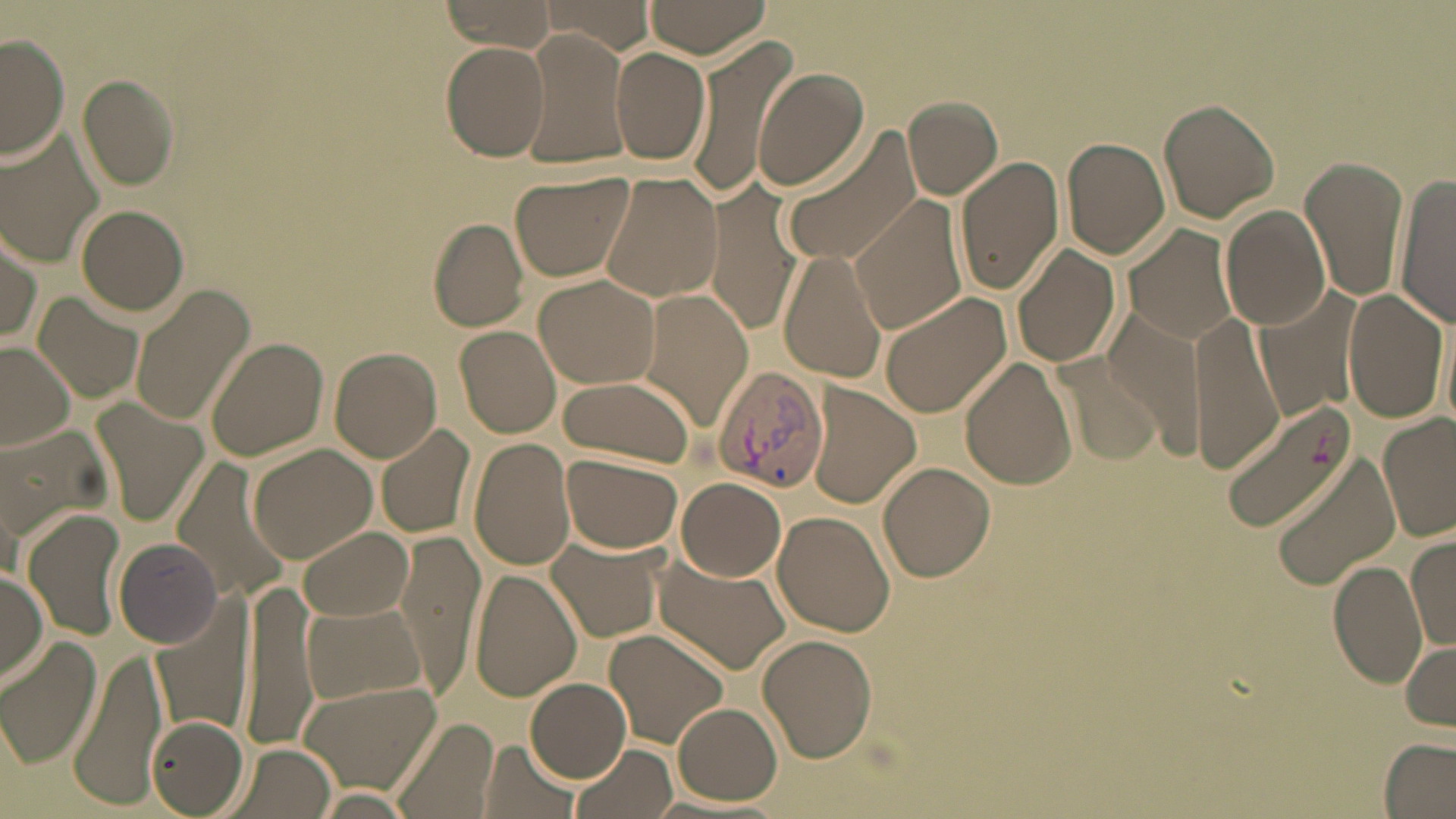

slide-level diagnosis = Plasmodium vivax
stain = May-Grünwald-Giemsa
uninfected red blood cell locations = approximate bounding boxes as [x1, y1, x2, y2] in pixels: [439, 0, 553, 55], [536, 0, 657, 53], [640, 0, 772, 58], [684, 31, 798, 204], [517, 33, 628, 170], [0, 34, 70, 162], [441, 42, 550, 160], [611, 49, 711, 166], [755, 68, 868, 191], [78, 73, 184, 190], [902, 96, 1002, 199], [1158, 100, 1278, 224], [777, 129, 925, 268], [0, 130, 107, 270], [1063, 138, 1169, 259], [1300, 154, 1408, 303], [955, 157, 1065, 294], [510, 169, 635, 282], [598, 173, 723, 302], [1394, 176, 1455, 328], [707, 183, 805, 336], [847, 196, 967, 335], [76, 205, 190, 316], [1223, 205, 1333, 331], [426, 218, 530, 331], [1122, 223, 1243, 344], [0, 228, 43, 346], [1011, 244, 1120, 369], [778, 249, 890, 384], [534, 275, 661, 389], [129, 283, 253, 426], [1255, 284, 1366, 422], [1341, 287, 1447, 430], [636, 289, 750, 427], [32, 292, 144, 405], [876, 292, 1011, 418], [1104, 308, 1208, 450], [1189, 311, 1284, 474], [454, 325, 563, 437], [205, 336, 329, 462], [0, 343, 76, 449], [330, 348, 444, 461], [1052, 350, 1161, 466], [959, 357, 1079, 490], [557, 376, 697, 466], [806, 383, 920, 508], [1222, 398, 1357, 534], [93, 400, 208, 525], [1377, 414, 1454, 543], [375, 422, 479, 540], [467, 436, 578, 572], [247, 443, 376, 562], [561, 453, 682, 555], [1270, 456, 1400, 591], [170, 458, 294, 605], [879, 461, 995, 583], [675, 477, 787, 582], [24, 509, 129, 640], [773, 511, 896, 637], [299, 527, 412, 623], [393, 528, 487, 699], [1406, 533, 1456, 653], [547, 536, 664, 646], [113, 539, 224, 648], [653, 557, 790, 674], [1327, 560, 1428, 690], [0, 566, 48, 685], [471, 569, 581, 700], [236, 577, 319, 750], [302, 602, 424, 705], [154, 604, 251, 741], [605, 628, 732, 748], [757, 633, 877, 762], [1, 635, 103, 769], [1400, 640, 1456, 731], [68, 645, 169, 807], [298, 675, 443, 791], [525, 678, 631, 781], [672, 703, 783, 805], [146, 715, 249, 816], [390, 716, 500, 819], [1380, 739, 1456, 817], [481, 740, 578, 819], [226, 741, 336, 819], [572, 745, 677, 819], [313, 790, 418, 819]
modality = light microscopy
image size = 1456×819 pixels
preparation = thin blood smear
magnification = 1000x
field of view = one of a larger specimen
Plasmodium vivax-infected red blood cell locations = approximate bounding boxes as [x1, y1, x2, y2] in pixels: [710, 364, 830, 494]